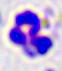
magnification = 400x
identification = white blood cell
modality = micrograph